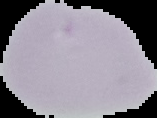
Summary:
  - Image size: 157×118 pixels
  - Image type: segmented cell region on a black background
  - Preparation: thin blood smear
  - Result: no malaria parasites detected